State which parasite is depicted.
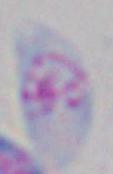
This is Toxoplasma gondii.

Captured at 1000x magnification. Micrograph.